Comment on the morphology of the red blood cells.
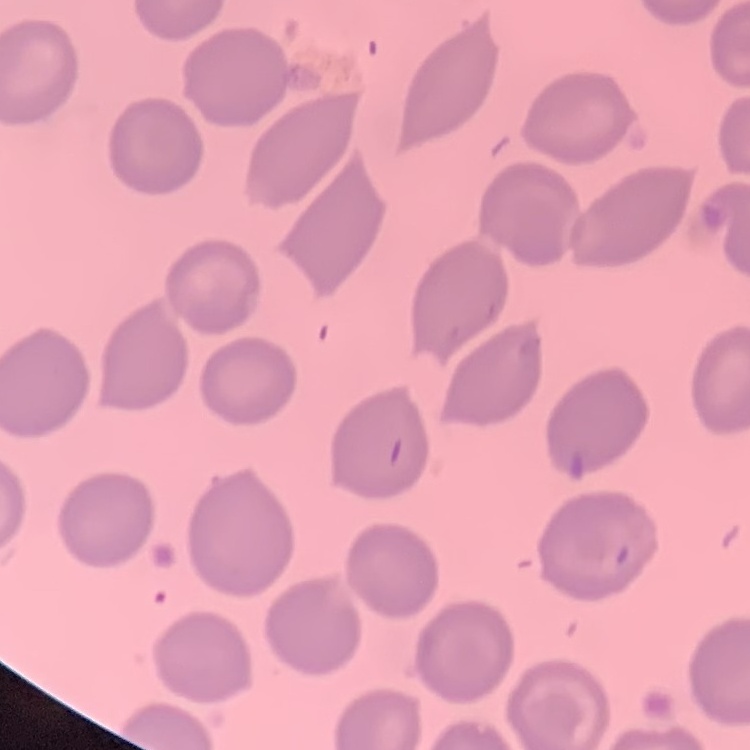

They show no rouleaux formation.

stain = Field's or Giemsa
image type = square crop of a larger photomicrograph
preparation = thin peripheral smear